Name the parasite shown.
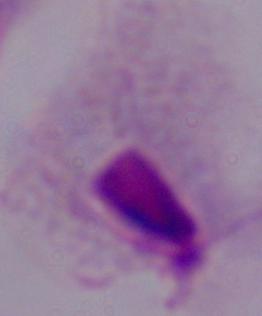

This is a trichomonad.

Micrograph. Captured at 1000x magnification.